Point out each Plasmodium parasite.
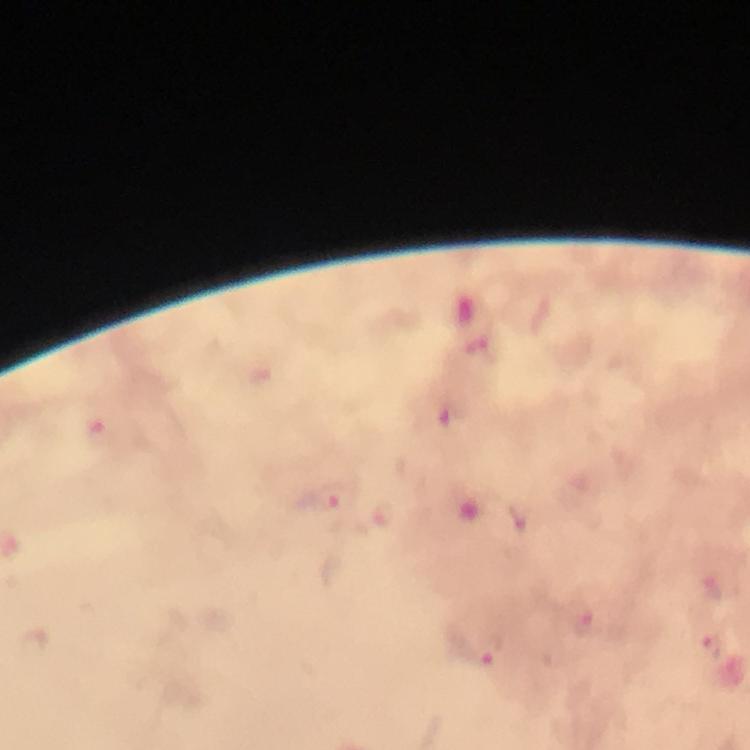
Approximate centers as [x, y] in pixels.
Plasmodium parasites: [264, 378], [100, 431], [333, 501].

Photographed through the microscope with a smartphone camera. Immersion oil applied. At 100x magnification. From a diagnostic examination for malaria. Thick smear. Cropped region of a single field of view. Image is 750×750 pixels. Giemsa stain.